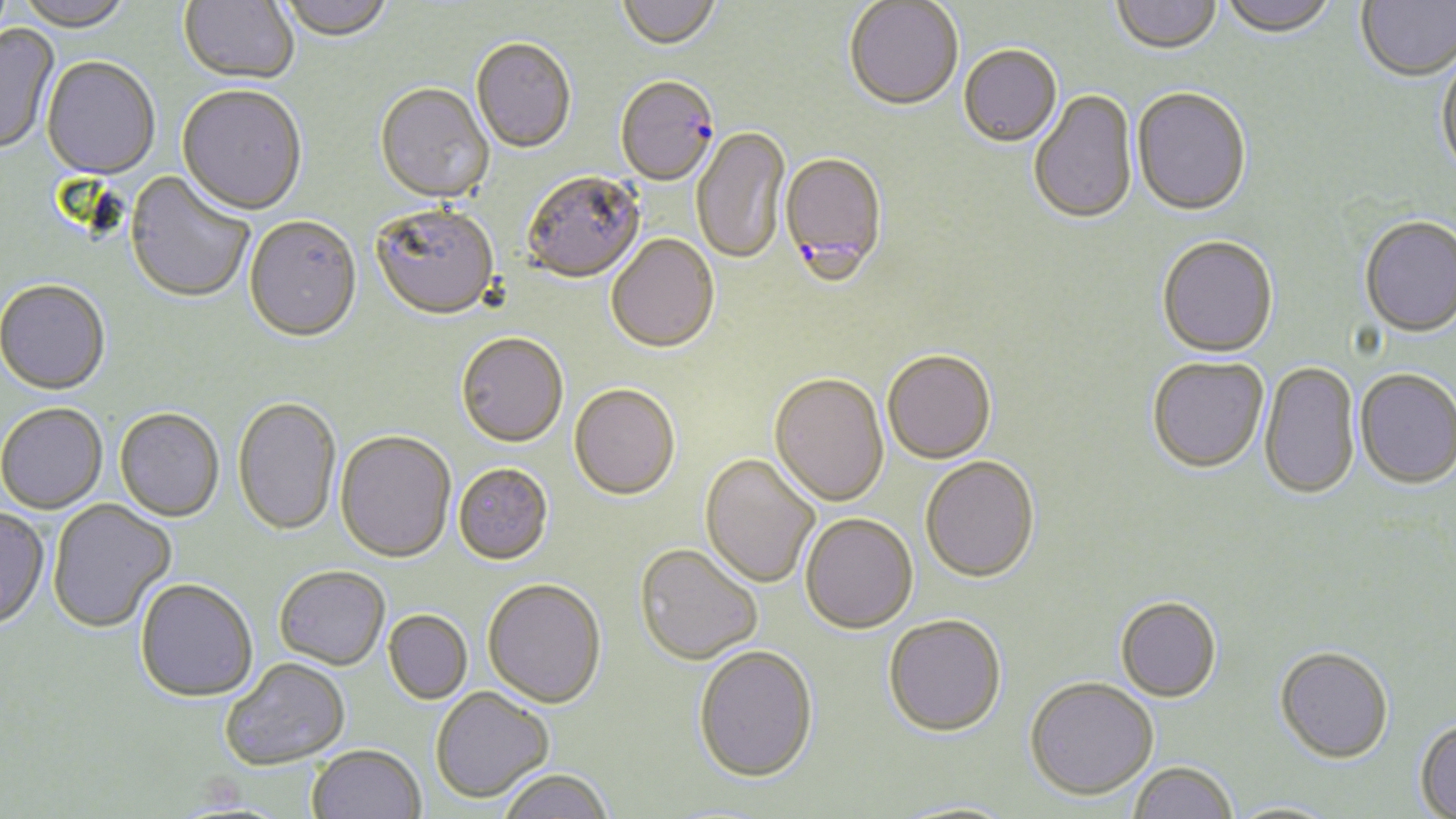 Approximate bounding boxes as (x1, y1, x2, y2) in pixels. Uninfected red blood cell locations: (16, 0, 133, 34), (178, 0, 299, 86), (276, 0, 395, 45), (617, 0, 720, 53), (1111, 0, 1222, 56), (1218, 0, 1337, 38), (1357, 0, 1456, 81), (844, 2, 963, 113), (0, 23, 59, 156), (471, 40, 576, 155), (959, 46, 1062, 149), (1436, 51, 1456, 177), (41, 58, 159, 181), (374, 84, 494, 206), (176, 87, 307, 218), (1132, 89, 1252, 218), (1029, 90, 1138, 228), (691, 126, 789, 266), (124, 172, 254, 305), (522, 174, 646, 285), (370, 207, 500, 323), (1359, 215, 1456, 337), (244, 218, 362, 345), (606, 236, 720, 356), (1157, 236, 1278, 358), (0, 281, 110, 396), (456, 335, 568, 449), (882, 352, 996, 466), (1147, 357, 1269, 473), (1259, 361, 1360, 501), (1355, 368, 1456, 488), (769, 376, 889, 509), (569, 386, 680, 503), (233, 398, 342, 538), (0, 404, 107, 515), (115, 408, 225, 523), (335, 432, 456, 565), (699, 455, 820, 590), (920, 458, 1040, 585), (453, 465, 553, 566), (47, 500, 176, 633), (0, 508, 49, 631), (800, 515, 918, 636), (634, 545, 762, 666), (274, 568, 390, 671), (134, 580, 258, 704), (482, 581, 607, 710), (1115, 597, 1222, 703), (383, 611, 472, 705), (883, 617, 1007, 739), (1275, 645, 1394, 763), (694, 648, 819, 785), (221, 659, 350, 770), (1025, 677, 1158, 801), (431, 687, 553, 802), (1415, 719, 1456, 818), (306, 745, 426, 819), (1128, 761, 1238, 819), (496, 769, 613, 819), (1223, 801, 1343, 819). Plasmodium falciparum-infected red blood cell locations: (615, 78, 720, 188), (780, 154, 889, 287). Slide-level diagnosis: Plasmodium falciparum. Light microscopy. Single field of view. Image is 1456×819 pixels. May-Grünwald-Giemsa stain. Thin blood smear. 1000x magnification.